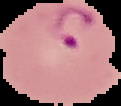

Image is 121×106 pixels. From a thin blood smear. Segmented cell region on a black background. Malaria status: parasitized.